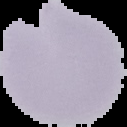

Summary:
  - Malaria status: parasitized
  - Image type: segmented cell region with the area outside set to black
  - Image size: 127×127 pixels
  - Preparation: thin blood film